Identify the parasite.
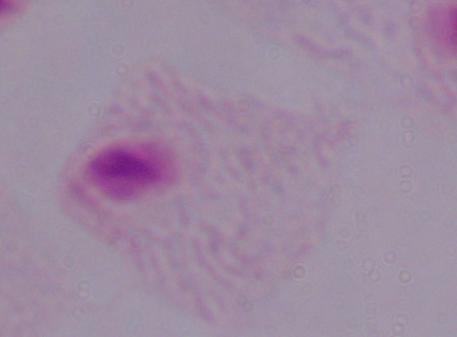
This is a trichomonad.

magnification = 1000x
modality = photomicrograph